Report the malaria status of this cell.
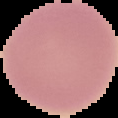

It is uninfected.

{
  "image_size": "118×118 pixels",
  "image_type": "cell region segmented out of the field of view; surrounding area masked to black",
  "preparation": "thin blood smear"
}